State which parasite is depicted.
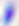

Toxoplasma gondii.

Summary:
  - Magnification: 400x
  - Modality: photomicrograph